Identify the parasite.
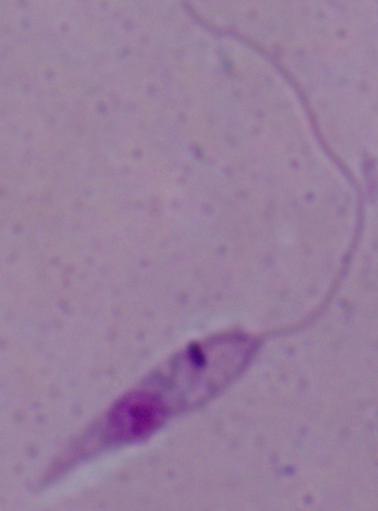

Leishmania.

Micrograph. Captured at 1000x magnification.